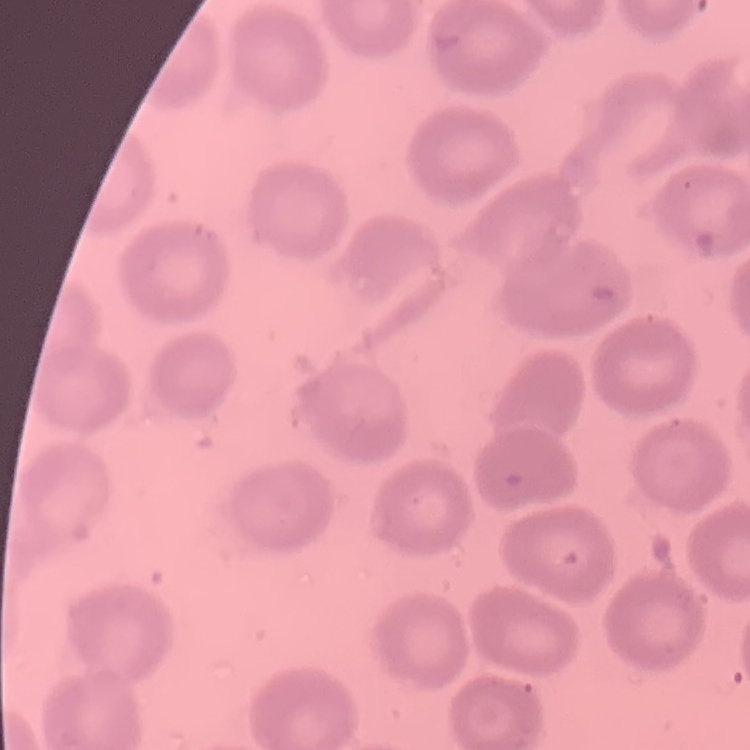
red_blood_cell_morphology: no rouleaux formation
preparation: thin peripheral smear
image_type: square crop of a larger photomicrograph
stain: Field's or Giemsa